Classify this cell by malaria status.
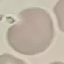
Uninfected.

Thin smear of blood. Photographed with a smartphone camera at the microscope eyepiece. Cell patch, automatically extracted from a larger field of view and resized to 64 × 64 pixels. Giemsa-stained preparation.